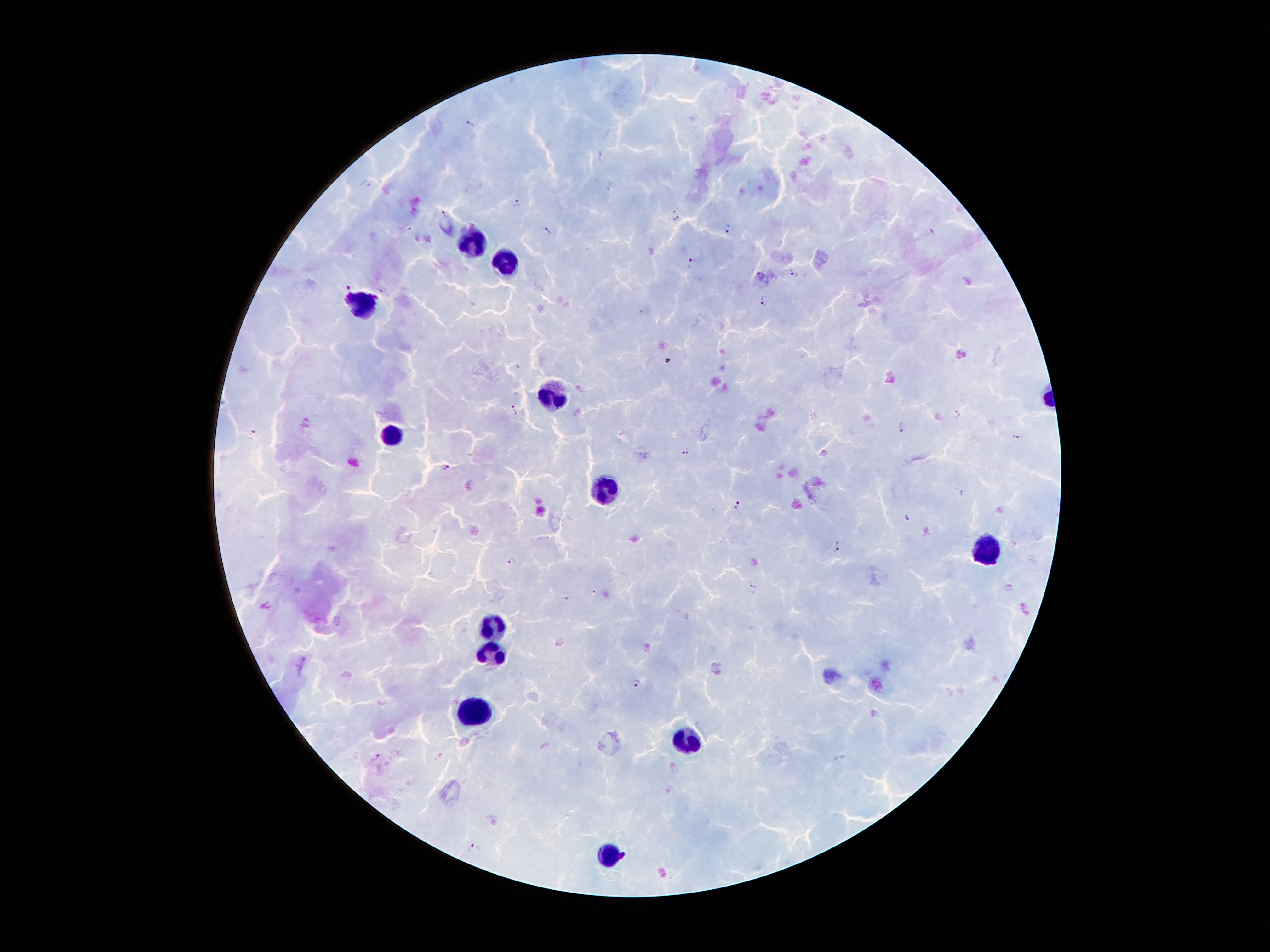
coordinate format = approximate centers as [x, y] in pixels
leukocyte locations = [475, 245], [506, 263], [365, 302], [561, 396], [394, 439], [608, 487], [992, 550], [495, 626], [486, 653], [474, 708], [686, 737], [608, 854]
malaria parasite locations = [469, 122], [601, 154], [366, 183], [516, 201], [445, 212], [676, 216], [409, 228], [728, 229], [930, 230], [546, 231], [692, 263], [793, 272], [760, 274], [383, 288], [765, 302], [513, 411], [959, 414], [901, 426], [254, 433], [1017, 437], [686, 451], [824, 453], [445, 466], [737, 505], [907, 516], [837, 545], [512, 560], [755, 588], [1010, 589], [566, 598], [636, 683], [375, 756], [473, 848]
image size = 1270×952 pixels
field of view = one from this slide
magnification = 100x
capture = smartphone camera through the microscope eyepiece
stain = Giemsa
patient malaria status = positive for Plasmodium falciparum
preparation = thick blood smear